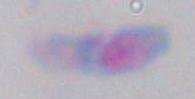
magnification = 1000x
identification = Toxoplasma gondii
modality = photomicrograph